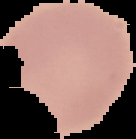

From a thin blood smear. Malaria status: uninfected. Image is 136×139 pixels. Cell region segmented out of the field of view; the surrounding area is masked to black.